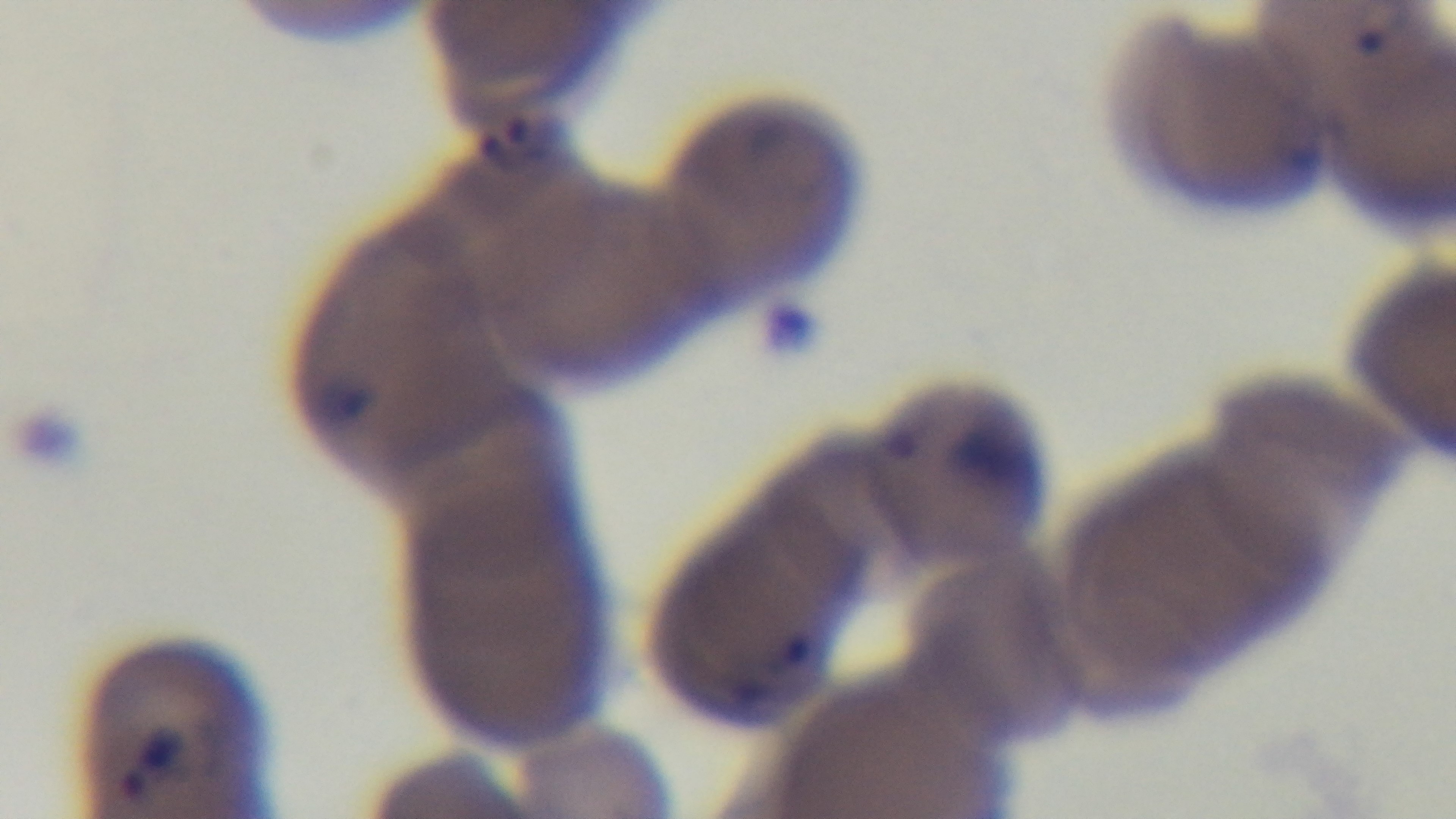
Summary:
  - Field of view: single
  - Malaria status: infected
  - Preparation: thin
  - Modality: light microscopy
  - Capture: mounted 4K digital camera
  - Objective: 100x oil immersion
  - Stain: Giemsa